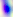

identification = Toxoplasma gondii
modality = photomicrograph
magnification = 400x